Locate the Plasmodium falciparum-infected red blood cells and any of indeterminate infection status.
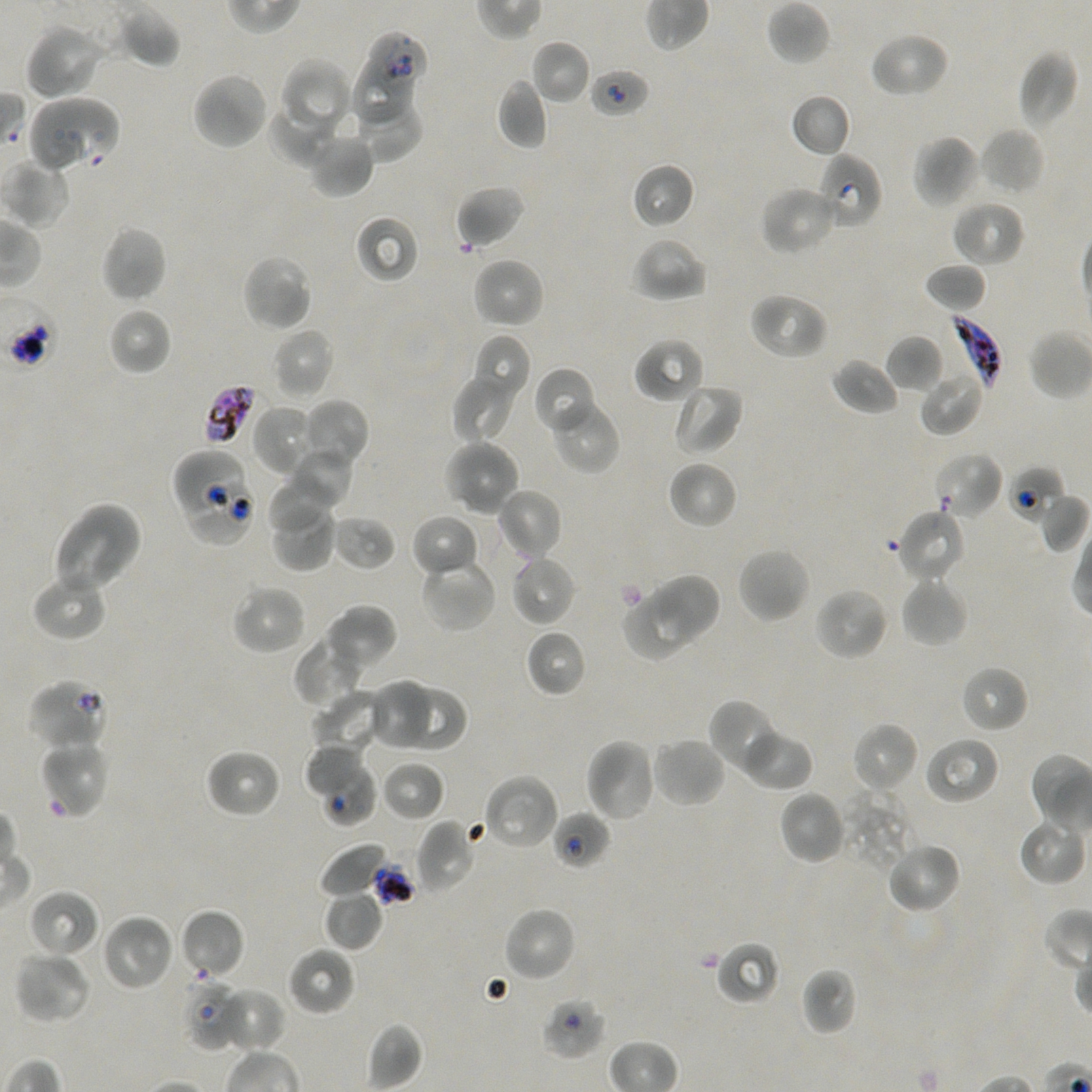
Approximate bounding boxes as (x1, y1, x2, y2) in pixels. Not every red blood cell is marked.
Infected red blood cells: (948, 315, 1003, 389).
Red blood cells of indeterminate infection status: (366, 33, 426, 95), (350, 59, 416, 122), (589, 67, 650, 119), (56, 95, 121, 172), (29, 98, 90, 175), (818, 151, 881, 230), (204, 384, 259, 446), (171, 447, 244, 517), (1007, 465, 1066, 522), (189, 481, 259, 547), (25, 678, 109, 752), (322, 765, 378, 826), (552, 810, 611, 870), (180, 976, 244, 1050), (540, 995, 607, 1061).

locations of uninfected red blood cells = (766, 1, 831, 65), (118, 6, 181, 69), (24, 23, 105, 101), (868, 31, 949, 99), (530, 39, 592, 105), (1018, 48, 1079, 132), (280, 58, 354, 138), (192, 71, 270, 151), (496, 79, 548, 149), (350, 90, 423, 161), (790, 93, 852, 158), (269, 101, 336, 166), (979, 126, 1046, 195), (306, 130, 374, 198), (911, 134, 982, 209), (1, 159, 71, 228), (632, 162, 695, 229), (455, 184, 526, 249), (759, 185, 839, 256), (951, 199, 1026, 268), (354, 213, 420, 284), (100, 225, 168, 304), (630, 236, 708, 303), (240, 253, 314, 331), (471, 257, 545, 329), (924, 261, 988, 313), (748, 291, 829, 361), (109, 306, 172, 376), (271, 327, 335, 400), (471, 335, 530, 406), (885, 335, 943, 393), (633, 338, 706, 404), (831, 358, 900, 416), (532, 365, 598, 435), (452, 368, 522, 443), (918, 368, 985, 436), (672, 382, 744, 456), (548, 397, 620, 474), (300, 399, 369, 469), (251, 403, 318, 476), (442, 439, 521, 517), (283, 446, 354, 512), (932, 451, 1004, 520), (667, 460, 738, 530), (268, 473, 335, 536), (495, 487, 563, 563), (1038, 491, 1089, 553), (268, 499, 337, 573), (52, 503, 143, 594), (894, 507, 968, 585), (410, 513, 479, 578), (331, 514, 397, 571), (736, 545, 811, 624), (509, 554, 577, 627), (419, 556, 498, 633), (31, 568, 109, 642), (653, 577, 721, 641), (900, 577, 968, 649), (230, 583, 308, 655), (814, 587, 890, 661), (624, 590, 697, 659), (323, 603, 398, 674), (525, 628, 587, 697), (294, 637, 363, 709), (959, 665, 1029, 733), (373, 680, 431, 747), (401, 683, 468, 750), (312, 689, 387, 756), (708, 699, 784, 775), (851, 721, 920, 795), (739, 727, 814, 791), (923, 735, 1000, 805), (650, 736, 727, 808), (584, 737, 659, 822), (39, 739, 111, 819), (306, 744, 366, 795), (204, 747, 282, 819), (380, 759, 445, 822), (481, 774, 560, 852), (840, 788, 915, 873), (777, 790, 848, 865), (1017, 816, 1087, 886), (416, 818, 479, 894), (884, 840, 962, 915), (318, 842, 391, 900), (27, 889, 100, 958), (323, 889, 384, 951), (502, 906, 577, 983), (179, 908, 244, 980), (100, 913, 175, 992), (716, 941, 781, 1005), (287, 946, 356, 1016), (14, 951, 92, 1025), (800, 966, 858, 1036), (213, 986, 287, 1054), (367, 1022, 422, 1091)
preparation = thin blood film
culture = static in-vitro Plasmodium falciparum strain NF54
image size = 1092×1092 pixels
objective = 100x, oil immersion, numerical aperture 1.45
stain = Giemsa
field of view = single
donor blood group = A+/O+